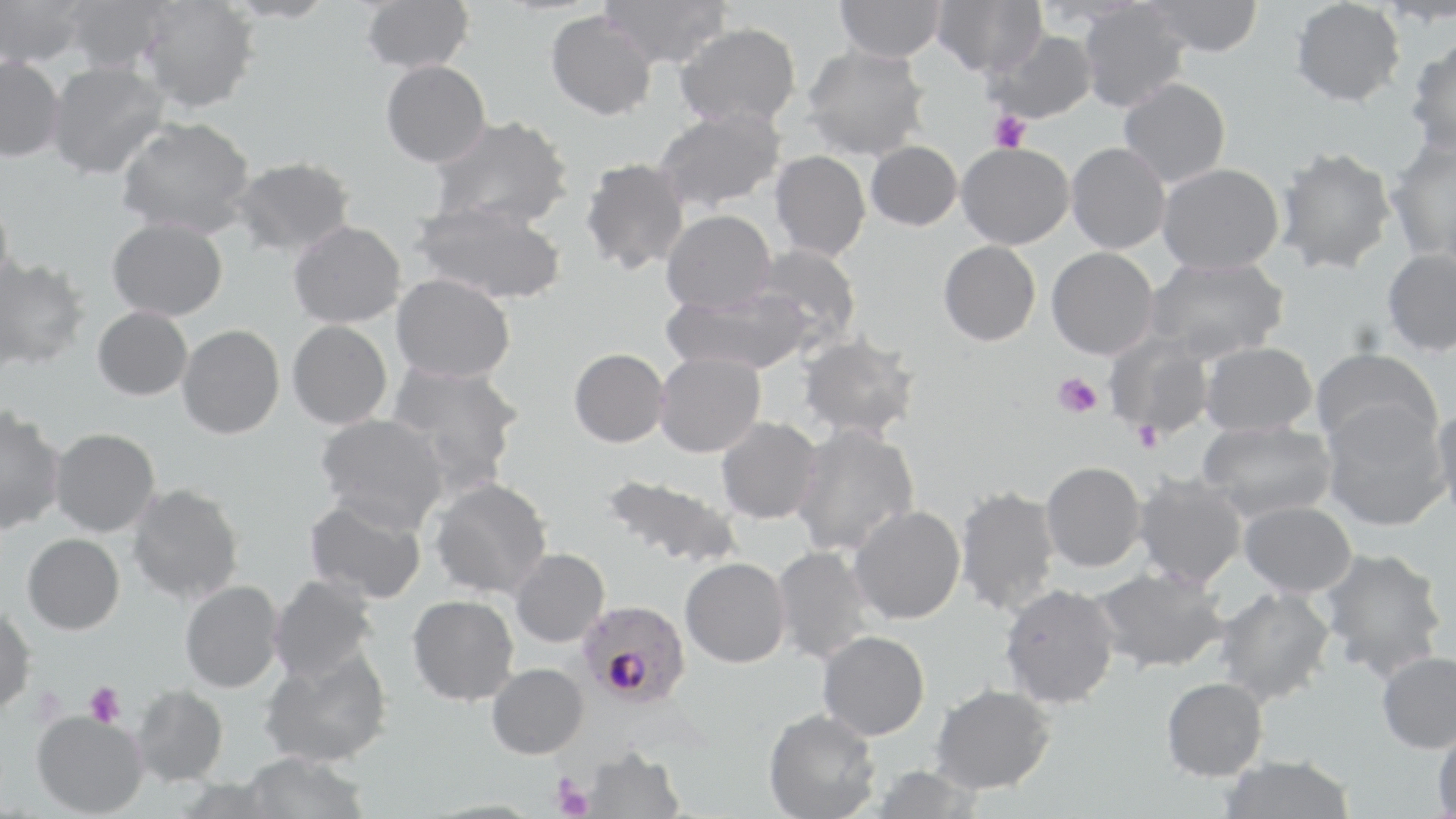

Approximate bounding boxes as [x1, y1, x2, y2] in pixels. Platelet locations: [989, 110, 1031, 152], [1053, 373, 1101, 418], [1134, 421, 1163, 452], [84, 682, 126, 728], [553, 778, 593, 818]. Plasmodium falciparum-infected red blood cell locations: [577, 599, 690, 707]. Uninfected red blood cell locations: [0, 0, 90, 67], [62, 0, 173, 74], [139, 0, 259, 113], [360, 0, 474, 74], [599, 0, 730, 68], [834, 0, 946, 62], [931, 0, 1047, 77], [1142, 0, 1263, 58], [1289, 0, 1405, 107], [1077, 3, 1189, 112], [546, 10, 657, 120], [675, 21, 802, 128], [984, 28, 1098, 124], [1406, 39, 1456, 160], [801, 44, 931, 160], [0, 56, 65, 162], [380, 60, 491, 167], [46, 61, 170, 180], [1118, 77, 1231, 188], [652, 106, 787, 212], [429, 115, 574, 230], [116, 116, 256, 238], [1385, 138, 1456, 262], [865, 140, 963, 231], [956, 142, 1075, 249], [1066, 142, 1171, 254], [1275, 145, 1398, 274], [770, 150, 871, 261], [230, 156, 356, 257], [580, 157, 691, 275], [1156, 163, 1284, 274], [0, 195, 14, 300], [411, 200, 568, 305], [661, 209, 776, 314], [107, 217, 228, 321], [289, 220, 406, 328], [938, 240, 1041, 346], [751, 244, 863, 347], [1046, 247, 1159, 360], [1381, 248, 1456, 356], [0, 255, 90, 372], [1145, 255, 1289, 362], [391, 273, 516, 383], [663, 285, 815, 376], [92, 306, 193, 400], [287, 320, 393, 430], [177, 324, 285, 439], [1104, 332, 1215, 439], [798, 333, 920, 441], [1199, 341, 1318, 436], [1311, 347, 1442, 450], [569, 348, 670, 447], [653, 352, 766, 457], [385, 361, 525, 487], [1322, 404, 1450, 531], [1431, 404, 1456, 522], [0, 406, 65, 535], [315, 413, 450, 531], [715, 416, 823, 524], [1197, 421, 1337, 520], [790, 422, 920, 556], [50, 427, 160, 537], [1041, 460, 1146, 572], [600, 472, 743, 569], [1133, 474, 1248, 589], [429, 477, 553, 600], [127, 483, 244, 603], [953, 485, 1061, 617], [304, 495, 428, 605], [1238, 500, 1357, 597], [848, 504, 966, 624], [22, 533, 124, 634], [771, 545, 877, 664], [1317, 546, 1448, 681], [510, 548, 609, 648], [680, 557, 790, 667], [1090, 566, 1230, 674], [269, 574, 379, 683], [180, 580, 284, 693], [999, 583, 1121, 709], [1215, 586, 1336, 705], [407, 594, 519, 706], [0, 606, 36, 713], [817, 630, 930, 740], [258, 647, 393, 768], [1377, 650, 1456, 754], [487, 662, 589, 758], [1160, 676, 1268, 780], [930, 683, 1056, 794], [131, 684, 229, 787], [763, 708, 881, 819], [32, 710, 148, 817], [1432, 724, 1456, 818], [579, 745, 685, 818], [241, 752, 370, 819], [1217, 756, 1355, 819], [865, 764, 983, 819]. Slide-level diagnosis: Plasmodium falciparum. One field of a larger specimen. Optical microscopy. Image is 1456×819 pixels. 1000x magnification. May-Grünwald-Giemsa-stained preparation. Thin blood smear.